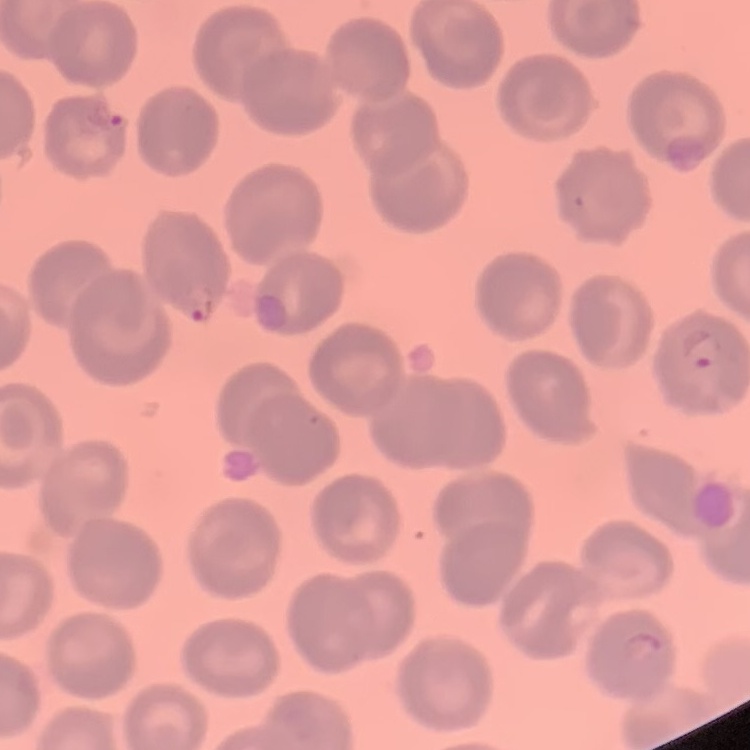

Summary:
  - Red blood cell morphology: no rouleaux formation
  - Image type: one tile cut from a larger photomicrograph
  - Preparation: thin blood film
  - Stain: Field's or Giemsa